Mark where cells are.
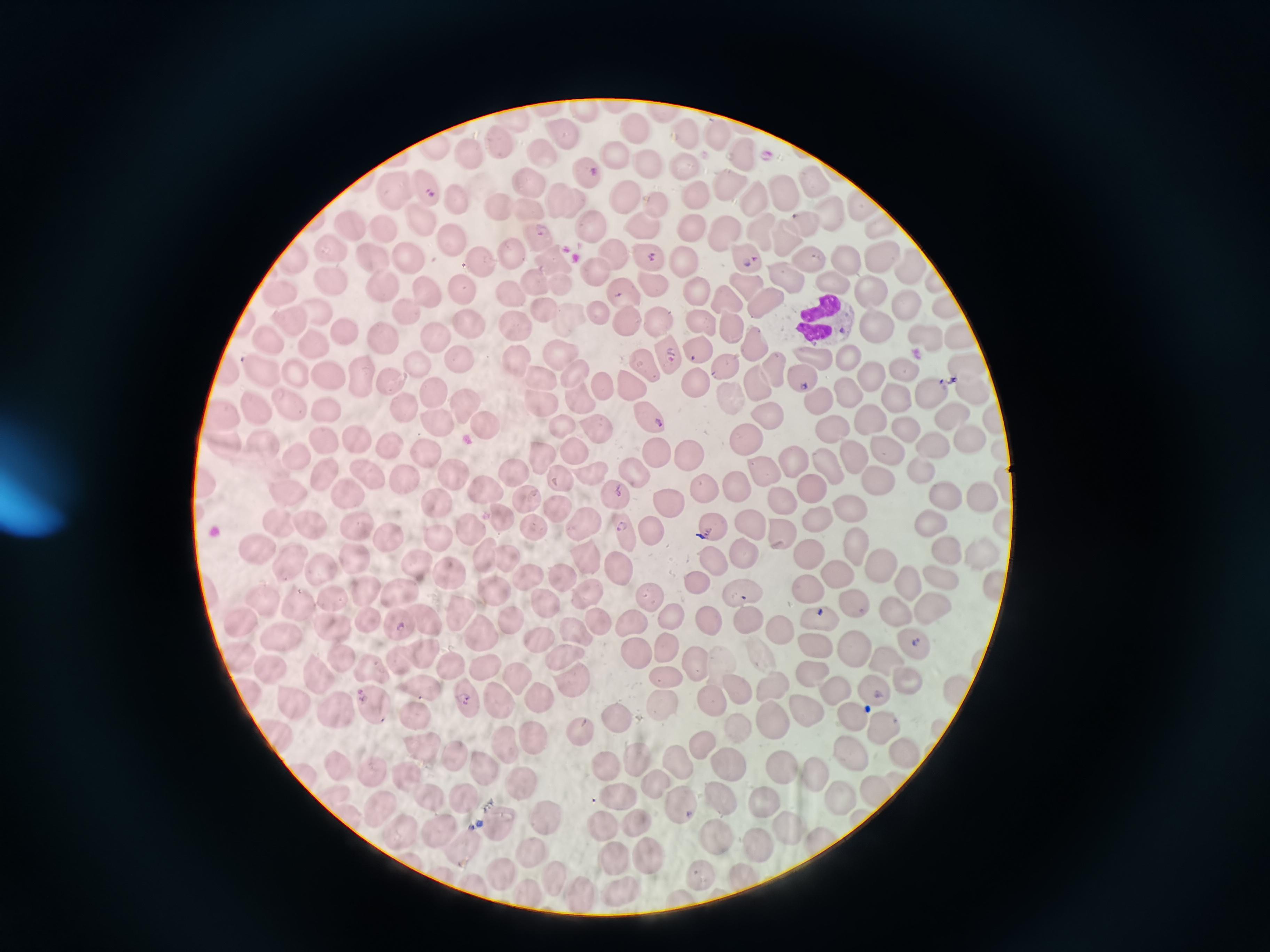
Approximate centers as [x, y] in pixels.
Cells: [583, 109], [513, 120], [636, 130], [715, 131], [684, 134], [564, 135], [500, 146], [469, 152], [742, 153], [613, 156], [541, 157], [646, 163], [683, 163], [727, 182], [814, 183], [528, 184], [782, 188], [395, 189], [428, 190], [755, 194], [626, 197], [696, 197], [457, 199], [565, 203], [657, 203], [499, 207], [526, 209], [829, 210], [422, 220], [805, 220], [592, 224], [646, 225], [690, 225], [354, 227], [386, 230], [759, 232], [723, 233], [536, 237], [786, 239], [455, 241], [332, 248], [611, 252], [510, 255], [647, 256], [741, 256], [805, 257], [879, 257], [288, 258], [409, 258], [373, 259], [549, 259], [845, 260], [480, 261], [685, 261], [912, 264], [592, 270], [785, 275], [832, 280], [333, 281], [535, 281], [558, 283], [748, 283], [380, 284], [654, 284], [693, 290], [870, 290], [461, 291], [281, 292], [427, 292], [622, 292], [507, 295], [726, 300], [764, 303], [541, 305], [905, 306], [945, 306], [318, 309], [594, 311], [568, 315], [407, 316], [514, 319], [626, 321], [659, 321], [286, 322], [703, 322], [728, 326], [874, 326], [468, 327], [341, 330], [429, 334], [268, 338], [923, 338], [383, 339], [961, 339], [757, 341], [313, 342], [558, 350], [699, 350], [848, 351], [673, 353], [514, 357], [458, 358], [812, 358], [416, 363], [645, 365], [725, 366], [258, 368], [964, 368], [905, 369], [779, 370], [327, 371], [291, 372], [572, 372], [868, 372], [538, 374], [360, 375], [798, 375], [387, 377], [692, 381], [602, 384], [758, 386], [627, 387], [968, 387], [430, 390], [844, 390], [895, 394], [928, 394], [577, 398], [734, 400], [540, 401], [816, 401], [465, 404], [400, 405], [286, 407], [256, 409], [319, 411], [649, 412], [948, 412], [222, 413], [992, 413], [769, 418], [869, 418], [434, 420], [484, 424], [831, 424], [594, 425], [562, 426], [906, 428], [965, 432], [742, 435], [323, 439], [356, 440], [223, 442], [928, 444], [388, 446], [263, 447], [883, 447], [571, 451], [653, 451], [425, 452], [685, 454], [849, 454], [541, 455], [294, 457], [793, 460], [826, 464], [916, 466], [588, 469], [629, 469], [758, 470], [449, 471], [509, 471], [327, 473], [366, 474], [878, 477], [405, 479], [559, 479], [1006, 482], [733, 483], [702, 485], [209, 486], [808, 486], [289, 489], [483, 489], [939, 492], [974, 492], [613, 493], [346, 494], [527, 497], [434, 500], [671, 501], [776, 501], [559, 505], [842, 505], [500, 515], [580, 519], [815, 520], [931, 520], [1004, 521], [280, 522], [747, 522], [303, 523], [533, 523], [356, 524], [709, 524], [467, 525], [655, 527], [622, 528], [387, 535], [435, 535], [783, 536], [946, 547], [745, 548], [858, 548], [255, 549], [482, 551], [506, 552], [982, 553], [351, 556], [808, 556], [585, 557], [713, 557], [291, 561], [417, 563], [615, 563], [882, 563], [317, 565], [837, 570], [939, 572], [448, 575], [527, 575], [568, 575], [702, 579], [995, 582], [909, 583], [488, 588], [804, 588], [365, 589], [401, 590], [738, 591], [584, 592], [647, 595], [331, 598], [264, 600], [852, 600], [548, 603], [301, 605], [457, 605], [893, 608], [929, 610], [669, 613], [705, 618], [748, 618], [820, 618], [238, 619], [425, 620], [632, 621], [396, 622], [512, 622], [371, 624], [593, 626], [331, 630], [575, 630], [783, 631], [481, 634], [277, 635], [911, 638], [542, 639], [672, 644], [819, 646], [423, 651], [563, 653], [637, 653], [857, 654], [396, 656], [719, 656], [235, 657], [342, 658], [887, 659], [697, 661], [450, 664], [371, 667], [489, 667], [266, 668], [810, 668], [513, 672], [907, 673], [319, 674], [665, 674], [732, 683], [772, 684], [570, 685], [873, 687], [957, 689], [833, 690], [421, 691], [245, 693], [462, 699], [538, 699], [289, 700], [492, 700], [708, 702], [659, 704], [374, 707], [800, 710], [337, 712], [413, 713], [848, 714], [612, 717], [775, 723], [878, 726], [578, 727], [733, 730], [530, 734], [277, 735], [699, 742], [423, 746], [502, 746], [848, 751], [901, 752], [448, 753], [677, 759], [633, 760], [473, 762], [336, 763], [777, 765], [602, 768], [722, 768], [810, 768], [300, 771], [368, 772], [405, 777], [521, 779], [655, 780], [872, 790], [618, 792], [332, 794], [427, 797], [458, 797], [837, 799], [764, 801], [718, 802], [377, 804], [675, 806], [344, 813], [541, 817], [502, 821], [631, 822], [791, 825], [603, 827], [395, 831], [436, 832], [823, 837], [712, 838], [468, 843], [758, 844], [532, 852], [650, 854], [612, 857], [697, 870], [499, 874], [552, 876], [742, 876], [473, 886], [620, 888], [524, 890], [572, 891].

Summary:
  - Malaria reading: positive
  - Field of view: single
  - Stain: Giemsa
  - Image size: 1270×952 pixels
  - Preparation: thin blood film
  - Capture: smartphone through the microscope eyepiece